Locate every leukocyte (white blood cell).
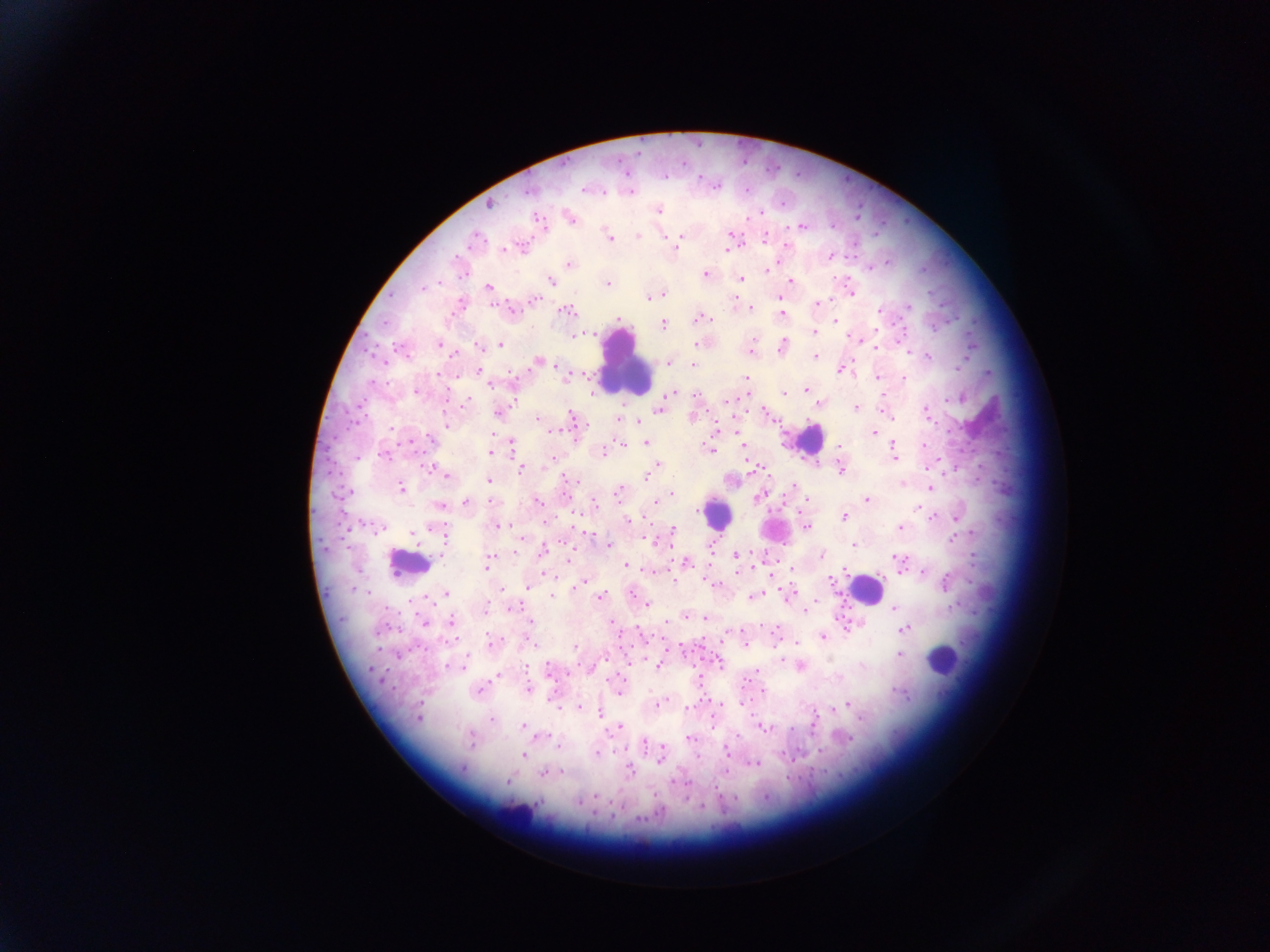

Approximate centers as [x, y] in pixels.
Leukocytes: [626, 364], [810, 439], [716, 514], [773, 528], [409, 563], [866, 589], [942, 659], [520, 812].

image size = 1270×952 pixels
capture = mobile-phone photograph through a microscope
field of view = single
preparation = thick blood film
malaria parasite locations = approximate centers as [x, y] in pixels: [528, 190], [584, 190], [631, 191], [604, 192], [488, 205], [658, 210], [570, 218], [537, 219], [801, 226], [730, 235], [638, 236], [681, 236], [763, 237], [474, 238], [663, 238], [609, 239], [677, 243], [786, 246], [521, 248], [676, 249], [504, 250], [726, 250], [830, 255], [569, 263], [870, 267], [768, 269], [706, 273], [741, 279], [551, 280], [791, 281], [608, 284], [489, 287], [423, 288], [663, 294], [851, 294], [648, 298], [535, 300], [817, 303], [909, 306], [750, 307], [510, 309], [567, 311], [879, 311], [781, 315], [699, 319], [835, 319], [618, 320], [663, 324], [814, 332], [581, 335], [752, 337], [857, 338], [438, 344], [695, 344], [500, 345], [478, 346], [782, 347], [876, 347], [750, 351], [907, 351], [453, 355], [814, 356], [928, 356], [540, 362], [669, 364], [693, 365], [959, 366], [839, 370], [479, 371], [438, 374], [876, 377], [746, 378], [903, 379], [490, 385], [806, 389], [416, 392], [783, 394], [670, 395], [696, 395], [728, 400], [948, 400], [466, 402], [817, 404], [856, 408], [660, 410], [499, 412], [765, 412], [927, 413], [890, 417], [573, 418], [618, 418], [537, 419], [637, 421], [448, 425], [391, 428], [874, 433], [431, 439], [409, 443], [511, 443], [646, 443], [622, 444], [744, 445], [893, 445], [924, 446], [840, 447], [709, 450], [491, 452], [604, 452], [384, 455], [893, 456], [940, 459], [551, 461], [657, 465], [925, 467], [429, 468], [522, 468], [650, 471], [840, 471], [447, 476], [647, 476], [488, 480], [571, 481], [902, 483], [794, 485], [931, 487], [400, 488], [618, 492], [347, 493], [671, 493], [758, 498], [808, 500], [866, 500], [490, 501], [536, 501], [466, 502], [595, 504], [440, 506], [918, 507], [845, 517], [934, 517], [955, 518], [628, 519], [499, 526], [381, 527], [807, 527], [901, 527], [673, 530], [445, 533], [588, 534], [972, 534], [413, 535], [952, 539], [654, 541], [608, 545], [854, 545], [710, 548], [543, 551], [516, 552], [736, 555], [820, 556], [569, 558], [897, 558], [487, 562], [687, 562], [901, 565], [626, 566], [792, 569], [845, 571], [738, 572], [923, 572], [900, 573], [830, 580], [582, 582], [946, 583], [712, 584], [579, 586], [528, 588], [501, 590], [446, 593], [631, 594], [552, 595], [601, 595], [752, 596], [816, 601], [647, 605], [513, 607], [893, 609], [486, 610], [806, 610], [685, 617], [705, 618], [529, 621], [451, 622], [424, 623], [612, 623], [905, 628], [823, 637], [490, 643], [797, 643], [530, 644], [745, 644], [576, 647], [681, 647], [899, 655], [781, 659], [720, 664], [658, 666], [862, 666], [462, 667], [548, 669], [373, 670], [757, 671], [497, 676], [697, 680], [528, 689], [479, 691], [763, 692], [619, 694], [902, 694], [551, 697], [742, 701], [657, 704], [720, 704], [847, 704], [687, 707], [579, 708], [833, 709], [600, 713], [419, 717], [862, 718], [492, 720], [712, 725], [522, 726], [620, 726], [762, 728], [791, 729], [545, 735], [689, 738], [850, 738], [470, 741], [644, 742], [558, 747], [821, 751], [726, 752], [596, 753], [661, 753], [523, 756], [697, 756], [660, 760], [755, 763], [462, 769], [629, 771], [726, 771], [562, 772], [543, 773], [507, 781], [595, 795], [578, 803], [703, 806]
country = Ghana